Locate every blood parasite and identify its species.
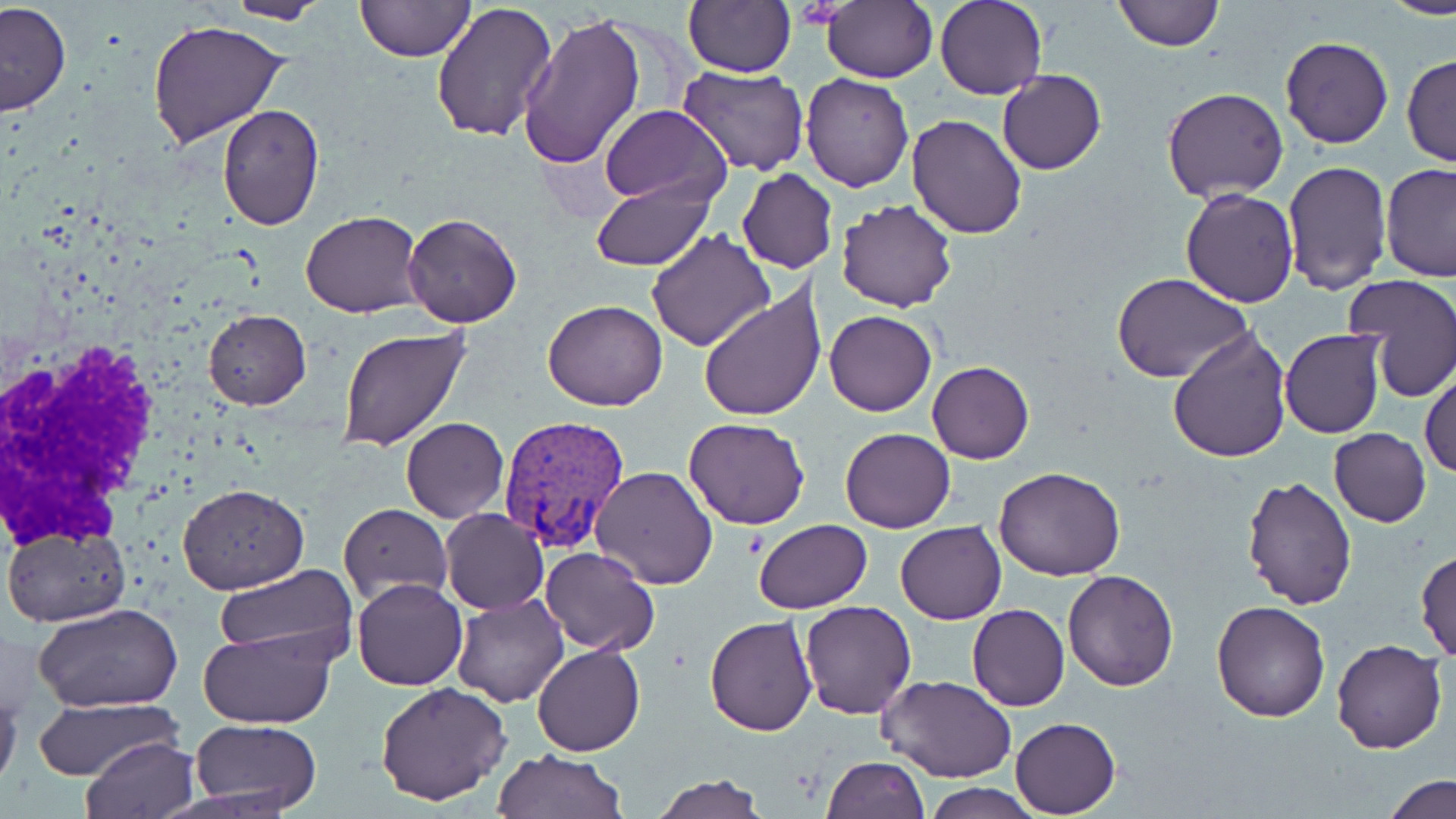

Approximate bounding boxes as (x1, y1, x2, y2) in pixels.
Plasmodium vivax-infected red blood cells: (497, 414, 630, 552).
No Plasmodium falciparum, Plasmodium ovale, Plasmodium malariae, Babesia divergens, or Trypanosoma brucei observed.

Summary:
  - Uninfected red blood cell locations: (224, 0, 331, 24), (354, 0, 474, 64), (683, 0, 795, 78), (823, 0, 938, 85), (935, 0, 1046, 101), (1113, 0, 1222, 51), (1379, 0, 1456, 19), (432, 1, 558, 142), (0, 3, 72, 117), (516, 10, 646, 171), (146, 18, 290, 148), (1280, 35, 1394, 149), (1403, 55, 1456, 168), (679, 64, 808, 175), (998, 70, 1106, 175), (800, 72, 913, 192), (1162, 86, 1289, 203), (216, 103, 325, 231), (601, 104, 730, 206), (907, 114, 1029, 239), (1282, 161, 1391, 295), (1381, 163, 1456, 282), (738, 168, 837, 275), (591, 180, 717, 270), (1181, 189, 1298, 307), (836, 199, 959, 312), (300, 210, 423, 317), (403, 212, 523, 328), (647, 227, 774, 351), (1114, 273, 1252, 385), (1344, 274, 1456, 403), (699, 287, 826, 422), (542, 299, 667, 413), (203, 310, 311, 409), (825, 310, 936, 416), (335, 326, 472, 452), (1168, 327, 1293, 465), (1280, 329, 1386, 438), (927, 360, 1035, 464), (1420, 368, 1455, 479), (401, 416, 509, 522), (685, 418, 812, 530), (839, 428, 954, 532), (1329, 428, 1431, 527), (994, 465, 1127, 581), (589, 466, 718, 588), (1240, 476, 1359, 610), (177, 484, 309, 593), (338, 505, 451, 605), (441, 508, 548, 614), (753, 517, 873, 614), (896, 521, 1005, 625), (2, 522, 131, 627), (540, 546, 660, 655), (1415, 548, 1456, 662), (215, 564, 357, 668), (1062, 570, 1179, 692), (352, 577, 468, 690), (453, 592, 568, 707), (799, 600, 918, 719), (1212, 600, 1331, 722), (967, 603, 1069, 711), (35, 604, 182, 714), (704, 614, 815, 736), (199, 628, 335, 727), (1331, 639, 1448, 753), (532, 644, 645, 756), (878, 673, 1016, 783), (0, 675, 22, 793), (375, 680, 514, 806), (33, 697, 178, 780), (1011, 717, 1120, 817), (190, 719, 322, 813), (81, 735, 199, 819), (493, 748, 627, 819), (822, 756, 930, 819), (651, 774, 767, 818), (1382, 775, 1455, 818), (922, 783, 1046, 818)
  - White blood cell locations: (1, 319, 158, 574)
  - Slide-level diagnosis: Plasmodium vivax
  - Modality: light microscopy
  - Magnification: 1000x
  - Stain: May-Grünwald-Giemsa
  - Field of view: single
  - Preparation: thin blood smear
  - Image size: 1456×819 pixels